Locate every leukocyte (white blood cell).
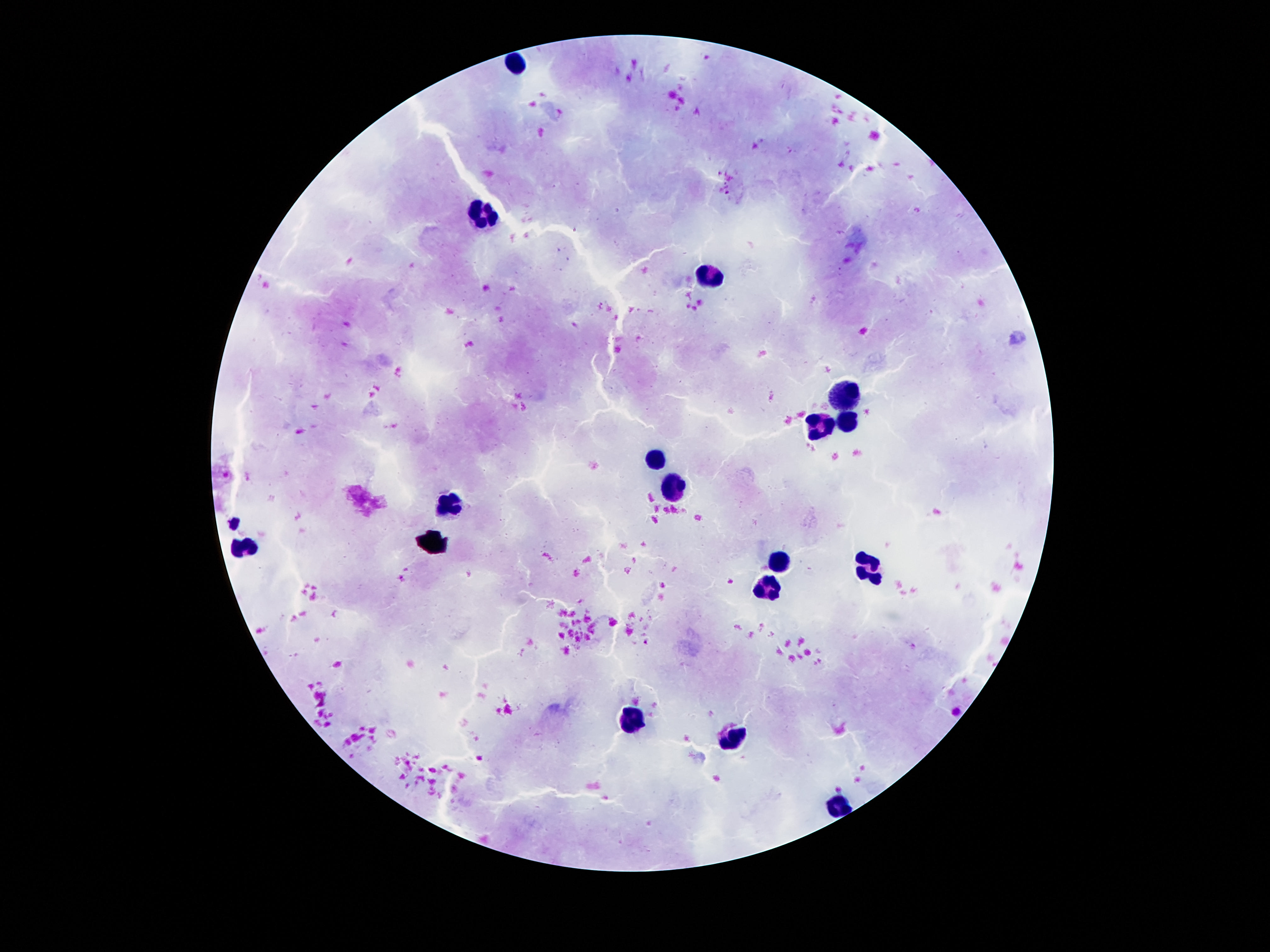

Approximate centers as {x, y} in pixels.
Leukocytes: {516, 65}, {486, 215}, {707, 279}, {844, 394}, {846, 421}, {822, 427}, {658, 458}, {678, 488}, {450, 505}, {243, 546}, {778, 561}, {866, 568}, {768, 579}, {631, 720}, {733, 739}, {839, 802}.

Image is 1270×952 pixels. 100x magnification. Smartphone photograph taken through the microscope eyepiece. Patient malaria status: uninfected. Giemsa-stained preparation. Thick peripheral-blood smear. Single field of view.